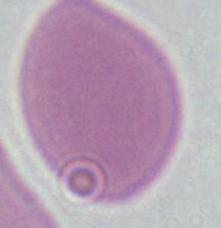

Summary:
  - Magnification: 1000x
  - Identification: erythrocyte
  - Modality: micrograph